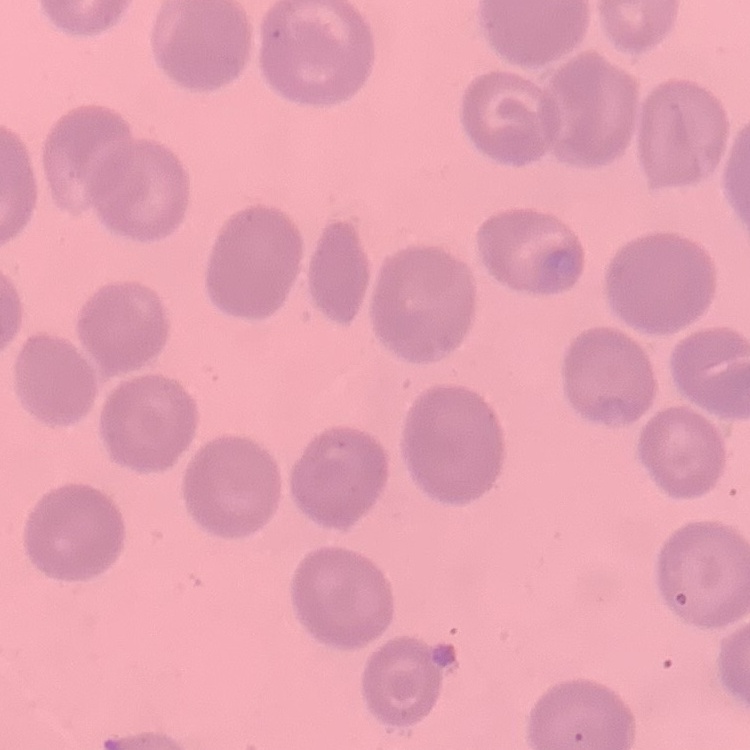

Summary:
  - Red blood cell morphology: no rouleaux formation
  - Stain: Field's or Giemsa
  - Preparation: thin peripheral smear
  - Image type: one tile cut from a larger photomicrograph